Classify this cell by malaria status.
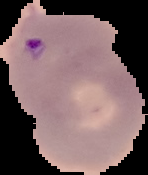

It is parasitized.

Summary:
  - Image size: 148×175 pixels
  - Preparation: thin blood film
  - Image type: segmented cell region on a black background